Point out each Plasmodium parasite.
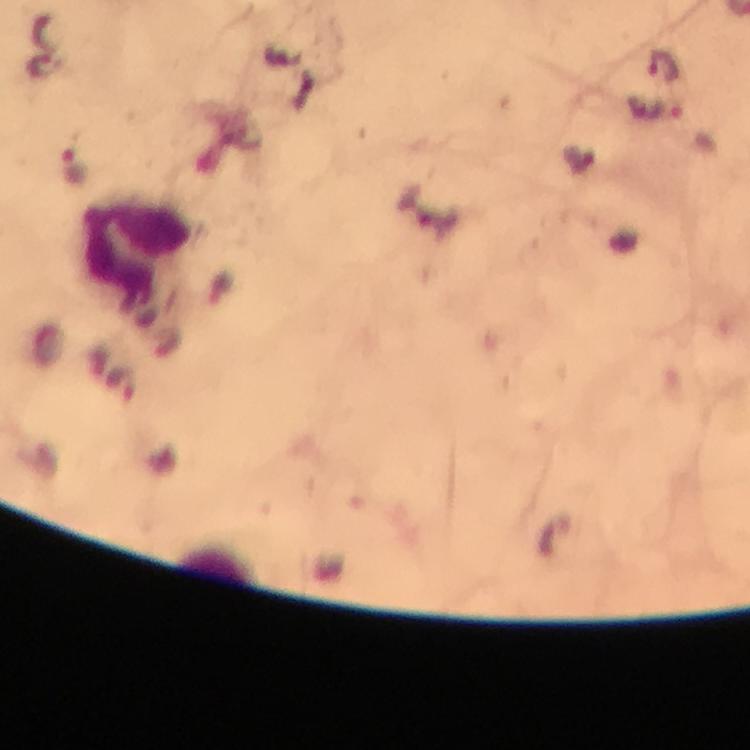
Approximate centers as [x, y] in pixels.
Plasmodium parasites: [665, 66], [73, 165].

magnification = 100x
cropped from = a single field of view
image size = 750×750 pixels
stain = Giemsa
preparation = thick smear
capture = smartphone camera through the microscope
context = from a malaria diagnostic workup
leukocyte locations = approximate centers as [x, y] in pixels: [136, 248]
immersion oil = used